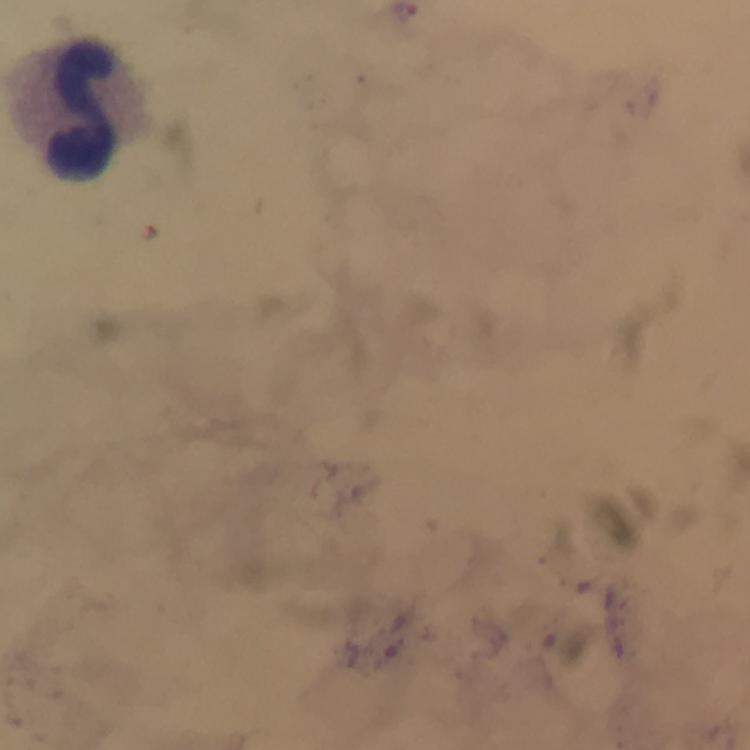

Approximate centers as [x, y] in pixels. Leukocyte locations: [73, 107]. Image is 750×750 pixels. Photographed through the microscope with a smartphone camera. Immersion oil was used. Thick blood smear. At 100x magnification. Plasmodium parasites: none seen. From a diagnostic examination for malaria. Giemsa-stained preparation. Cropped region of a single field of view.